Comment on the morphology of the red blood cells.
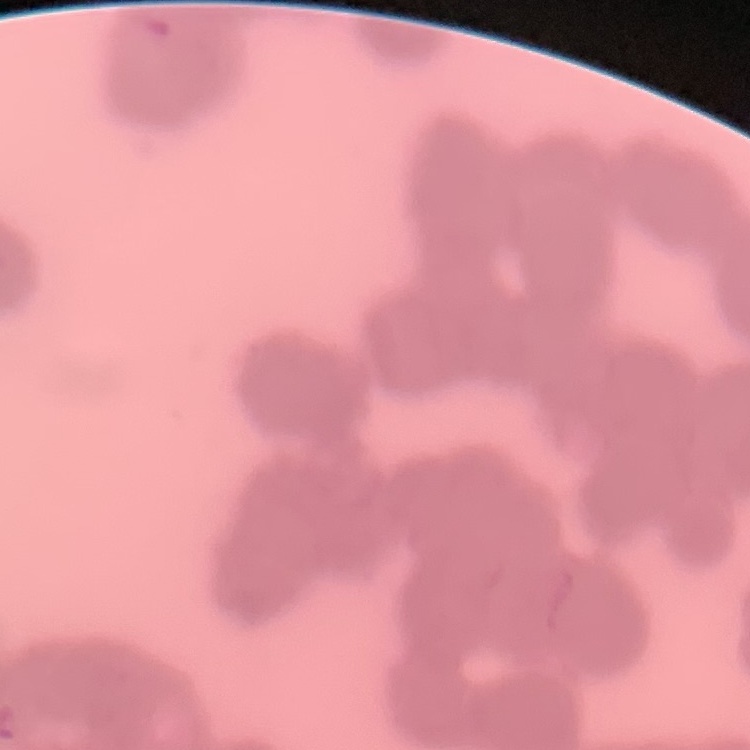
They show rouleaux formation.

Summary:
  - Image type: square crop of a larger photomicrograph
  - Stain: Field's or Giemsa
  - Preparation: thin peripheral smear